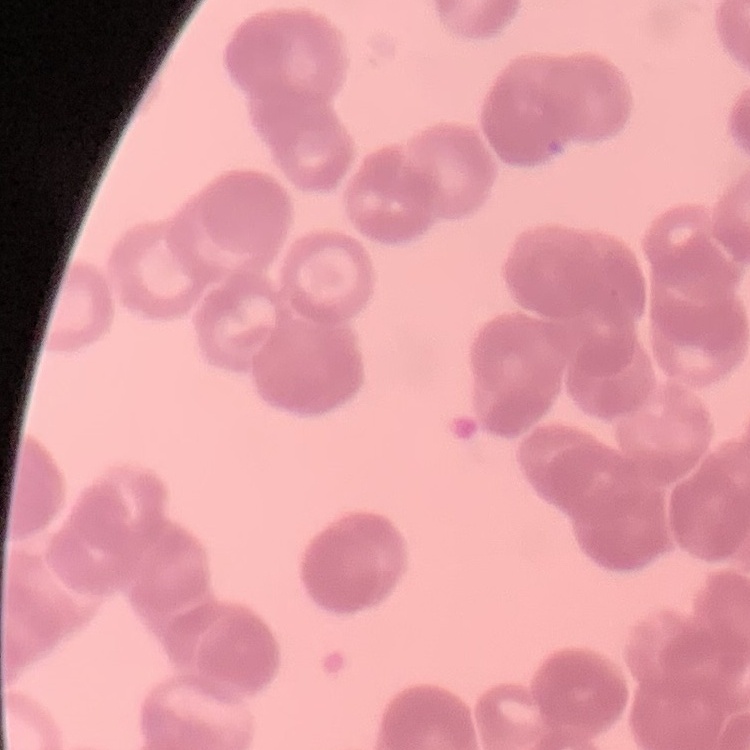

red blood cell morphology = rouleaux formation
image type = square crop of a larger photomicrograph
stain = Field's or Giemsa
preparation = thin blood film